Locate every blood parasite and identify its species.
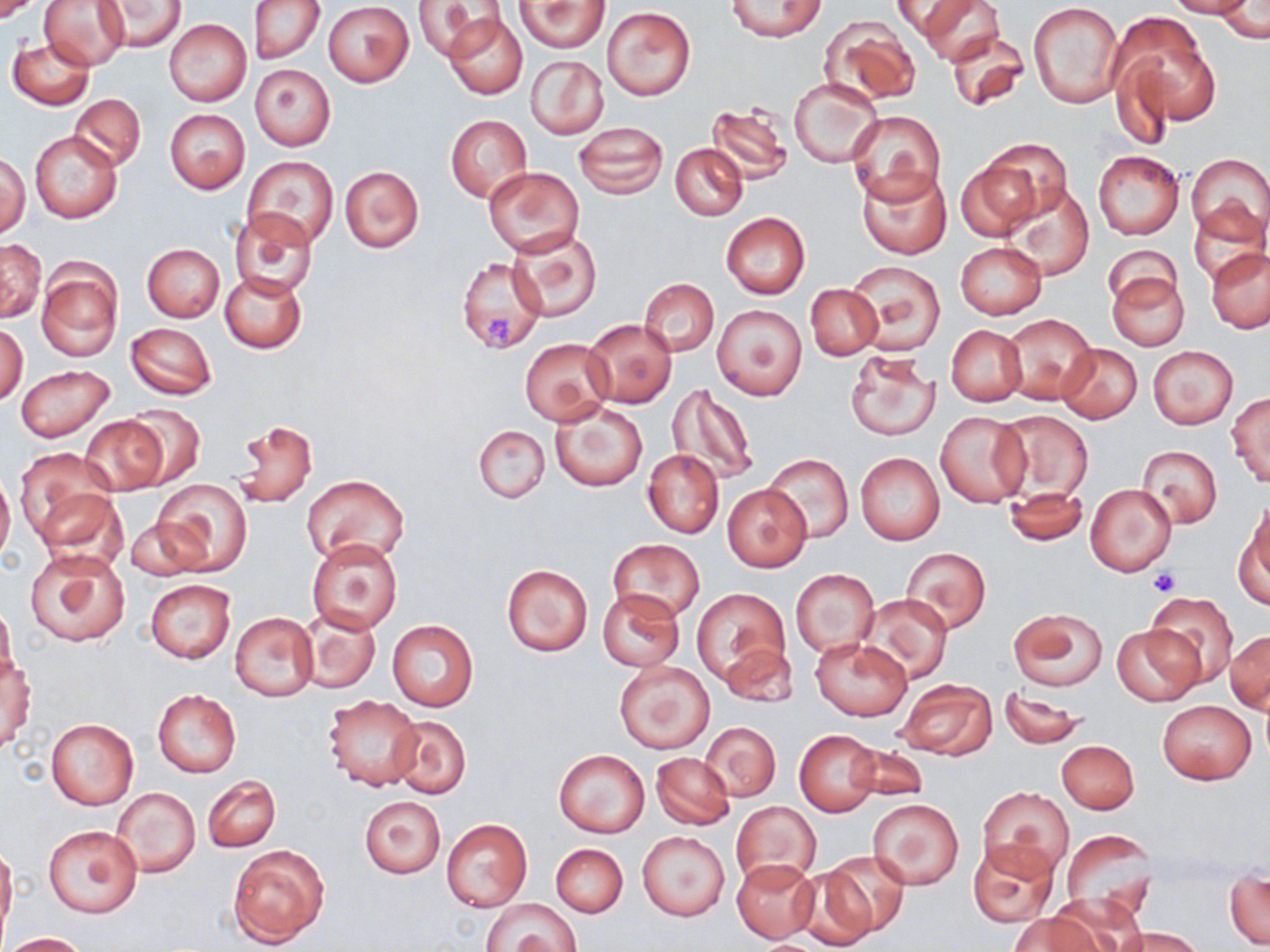
No blood parasites observed.

Summary:
  - Coordinate format: approximate bounding boxes as (x1, y1, x2, y2) in pixels
  - Uninfected red blood cell locations: (0, 0, 44, 22), (39, 0, 129, 69), (248, 0, 325, 65), (414, 0, 498, 60), (724, 0, 829, 41), (917, 0, 1002, 64), (1167, 0, 1256, 19), (100, 1, 186, 52), (515, 1, 609, 52), (894, 1, 968, 38), (1028, 1, 1124, 108), (323, 2, 414, 86), (1212, 5, 1268, 43), (602, 6, 697, 100), (443, 11, 528, 100), (1114, 12, 1219, 133), (818, 19, 921, 107), (165, 20, 251, 106), (945, 29, 1030, 111), (8, 36, 94, 109), (526, 56, 609, 139), (250, 64, 335, 149), (791, 78, 881, 166), (69, 93, 146, 172), (708, 100, 792, 182), (165, 109, 250, 194), (847, 111, 945, 205), (445, 116, 532, 202), (573, 121, 667, 197), (30, 130, 122, 223), (980, 137, 1073, 228), (672, 144, 747, 220), (1093, 149, 1183, 240), (1186, 152, 1270, 241), (1, 154, 29, 238), (956, 155, 1045, 239), (242, 156, 339, 248), (340, 166, 423, 252), (483, 166, 583, 257), (858, 167, 952, 259), (1002, 185, 1094, 279), (1188, 201, 1267, 285), (229, 210, 318, 298), (721, 212, 809, 300), (508, 228, 603, 323), (0, 239, 46, 322), (956, 242, 1047, 320), (142, 243, 224, 321), (1103, 245, 1181, 310), (1207, 249, 1270, 333), (457, 256, 548, 354), (37, 258, 123, 362), (847, 261, 945, 355), (1105, 270, 1189, 351), (220, 271, 306, 353), (639, 279, 718, 355), (805, 283, 883, 359), (712, 305, 807, 401), (1002, 314, 1098, 406), (583, 318, 677, 408), (125, 322, 217, 400), (1, 324, 27, 405), (947, 325, 1025, 406), (519, 338, 615, 426), (1056, 343, 1142, 422), (1147, 345, 1238, 428), (844, 350, 941, 443), (16, 364, 115, 442), (669, 384, 758, 485), (1228, 391, 1270, 486), (551, 403, 647, 491), (121, 405, 207, 489), (995, 411, 1094, 503), (936, 412, 1030, 508), (81, 416, 167, 496), (230, 421, 317, 508), (475, 424, 550, 503), (1136, 444, 1222, 529), (643, 449, 724, 538), (18, 450, 117, 548), (762, 452, 852, 544), (856, 452, 944, 545), (0, 469, 15, 570), (301, 474, 410, 566), (153, 479, 252, 576), (1085, 483, 1177, 577), (723, 485, 809, 571), (1004, 487, 1088, 546), (1237, 510, 1270, 608), (124, 516, 209, 583), (608, 538, 705, 625), (307, 539, 403, 633), (26, 545, 128, 648), (901, 547, 991, 634), (501, 563, 593, 656), (790, 569, 879, 658), (145, 579, 235, 662), (599, 589, 683, 670), (692, 589, 788, 688), (859, 592, 952, 682), (1145, 592, 1238, 684), (0, 605, 17, 685), (297, 608, 380, 694), (1010, 608, 1108, 691), (229, 611, 317, 701), (387, 621, 478, 711), (1112, 623, 1203, 707), (1227, 629, 1270, 714), (811, 637, 912, 721), (719, 643, 797, 709), (1, 656, 34, 753), (613, 659, 715, 755), (896, 678, 996, 760), (999, 687, 1088, 749), (153, 690, 240, 777), (323, 694, 424, 791), (1158, 700, 1255, 784), (386, 715, 471, 800), (46, 719, 138, 809), (700, 722, 780, 801), (795, 730, 883, 816), (1057, 740, 1139, 814), (845, 742, 928, 804), (554, 750, 649, 836), (651, 752, 734, 830), (203, 776, 280, 853), (978, 785, 1072, 879), (111, 786, 199, 879), (359, 795, 445, 878), (868, 799, 964, 890), (732, 801, 820, 887), (440, 817, 532, 911), (44, 824, 142, 918), (1059, 830, 1157, 923), (637, 831, 729, 922), (967, 840, 1061, 929), (227, 842, 331, 949), (551, 843, 627, 917), (0, 844, 17, 935), (813, 850, 912, 940), (732, 859, 820, 943), (1226, 867, 1268, 949), (792, 872, 877, 948), (481, 898, 582, 952), (1038, 898, 1139, 952), (1010, 913, 1103, 952), (1119, 928, 1203, 952), (1, 932, 88, 951)
  - Platelet locations: (483, 315, 515, 350), (1147, 567, 1180, 596)
  - Slide-level diagnosis: no evidence of blood parasites
  - Modality: light microscopy
  - Magnification: 1000x
  - Image size: 1270×952 pixels
  - Stain: May-Grünwald-Giemsa
  - Field of view: single
  - Preparation: thin blood smear